State the blood parasite species.
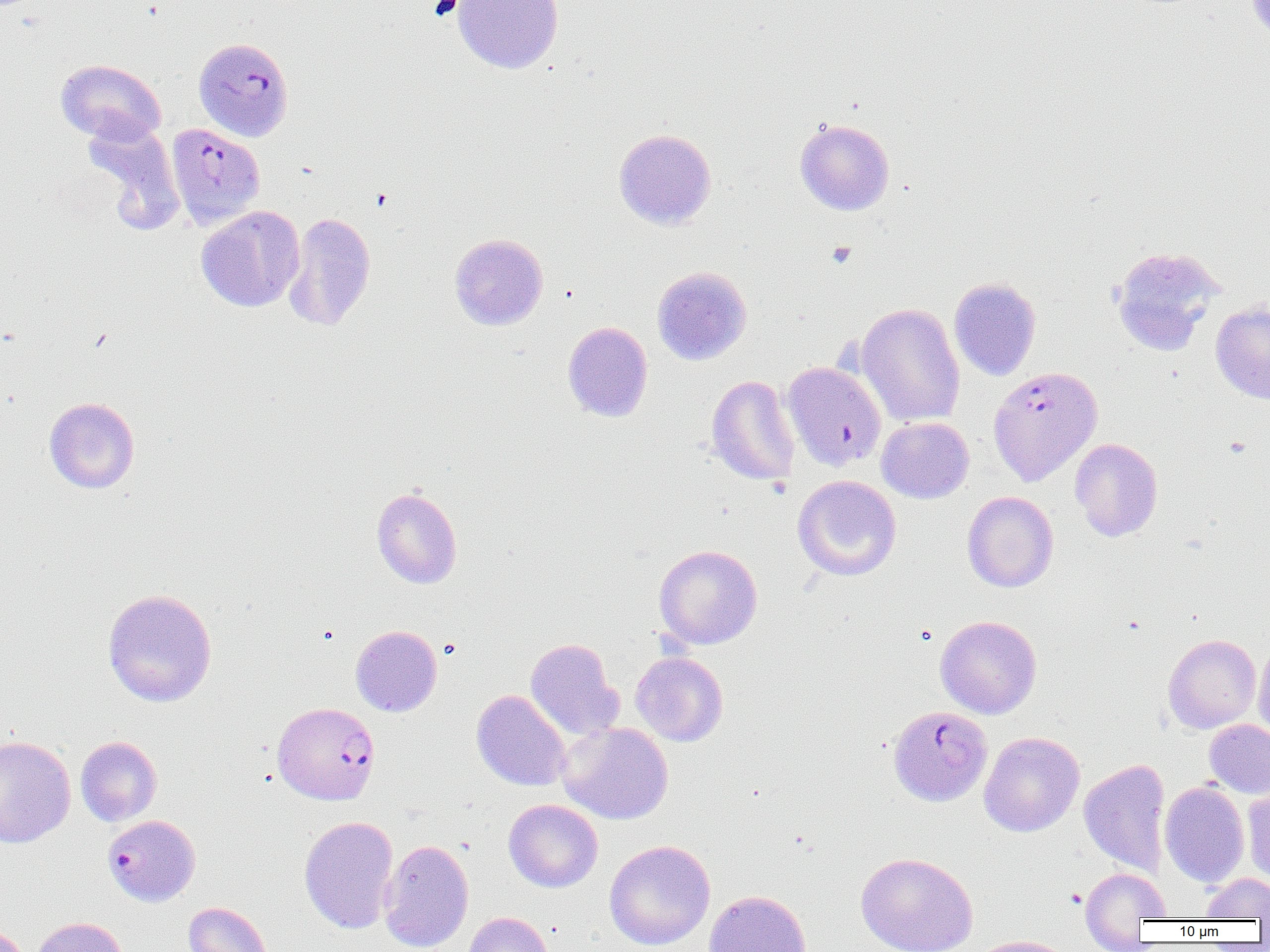

Plasmodium falciparum.

Approximate bounding boxes as [x1, y1, x2, y2] in pixels. Plasmodium falciparum-infected red blood cell locations: [193, 37, 294, 141], [166, 123, 265, 229], [782, 361, 886, 471], [988, 366, 1103, 486], [272, 699, 380, 808], [888, 705, 993, 806], [102, 814, 201, 907]. Platelet locations: [826, 241, 856, 269]. Uninfected red blood cell locations: [453, 0, 563, 74], [1246, 1, 1270, 40], [56, 59, 166, 144], [82, 116, 185, 235], [794, 118, 895, 215], [613, 128, 716, 230], [196, 206, 304, 312], [284, 212, 377, 331], [449, 233, 548, 330], [1109, 245, 1225, 355], [652, 266, 752, 365], [949, 278, 1041, 380], [1211, 301, 1270, 404], [856, 303, 965, 427], [563, 321, 653, 422], [706, 374, 800, 486], [44, 397, 139, 493], [876, 417, 974, 503], [1070, 438, 1163, 542], [793, 475, 902, 581], [371, 487, 462, 588], [962, 491, 1059, 592], [653, 544, 763, 649], [102, 588, 217, 707], [934, 615, 1042, 719], [351, 625, 442, 717], [1163, 634, 1261, 733], [525, 638, 623, 741], [1253, 638, 1270, 742], [631, 651, 728, 746], [471, 689, 571, 791], [1204, 719, 1270, 798], [557, 722, 674, 824], [978, 731, 1084, 837], [0, 735, 76, 848], [75, 735, 162, 826], [1079, 759, 1170, 877], [1160, 781, 1249, 887], [1243, 785, 1270, 886], [503, 799, 603, 892], [298, 815, 399, 934], [379, 838, 474, 952], [604, 840, 716, 950], [856, 851, 978, 952], [1080, 868, 1170, 936], [1200, 873, 1270, 919], [704, 890, 813, 952], [183, 902, 272, 952], [462, 912, 553, 952], [30, 916, 129, 952], [967, 935, 1077, 952]. Image is 1270×952 pixels. Thin blood smear. 1000x magnification. One field of a larger specimen. Optical microscopy.